Report the malaria status of this cell.
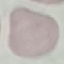
Uninfected.

Summary:
  - Image type: cell patch, automatically extracted from a larger field of view and resized to 64 × 64 pixels
  - Stain: Giemsa
  - Capture: smartphone through the microscope eyepiece
  - Preparation: thin blood film